Locate and identify every blood parasite.
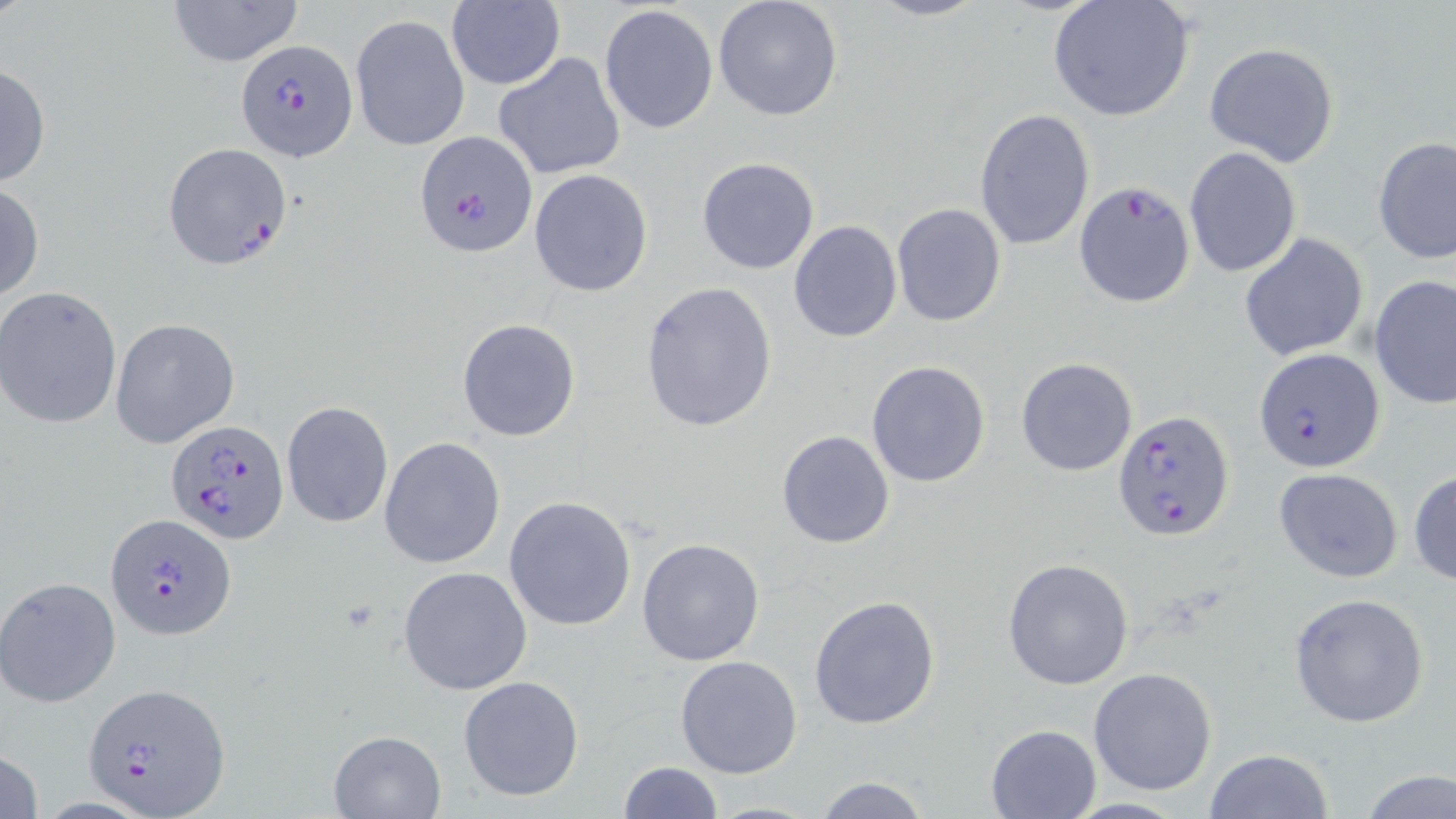
Approximate bounding boxes as named x1/y1/x2/y2 corners in pixels.
Plasmodium falciparum-infected red blood cells: (x1=235, y1=39, x2=357, y2=160), (x1=414, y1=131, x2=539, y2=259), (x1=160, y1=138, x2=292, y2=270), (x1=1074, y1=180, x2=1195, y2=306), (x1=1254, y1=347, x2=1386, y2=473), (x1=1113, y1=409, x2=1234, y2=540), (x1=166, y1=418, x2=290, y2=543), (x1=104, y1=512, x2=234, y2=641), (x1=83, y1=681, x2=230, y2=817).
No Plasmodium ovale, Plasmodium malariae, Plasmodium vivax, Babesia divergens, or Trypanosoma brucei observed.

Summary:
  - Uninfected red blood cell locations: (x1=167, y1=0, x2=305, y2=68), (x1=713, y1=0, x2=843, y2=123), (x1=864, y1=0, x2=987, y2=22), (x1=1047, y1=0, x2=1196, y2=124), (x1=446, y1=1, x2=564, y2=90), (x1=600, y1=4, x2=718, y2=135), (x1=350, y1=13, x2=470, y2=152), (x1=1203, y1=42, x2=1339, y2=168), (x1=493, y1=51, x2=626, y2=180), (x1=0, y1=63, x2=50, y2=188), (x1=974, y1=108, x2=1094, y2=252), (x1=1372, y1=136, x2=1455, y2=264), (x1=1184, y1=147, x2=1302, y2=278), (x1=696, y1=156, x2=821, y2=275), (x1=528, y1=168, x2=654, y2=297), (x1=0, y1=182, x2=45, y2=304), (x1=891, y1=203, x2=1006, y2=325), (x1=788, y1=220, x2=902, y2=341), (x1=1239, y1=232, x2=1369, y2=361), (x1=1369, y1=276, x2=1456, y2=410), (x1=639, y1=281, x2=776, y2=432), (x1=0, y1=285, x2=123, y2=431), (x1=108, y1=318, x2=240, y2=447), (x1=456, y1=318, x2=581, y2=442), (x1=1016, y1=357, x2=1138, y2=477), (x1=866, y1=359, x2=993, y2=488), (x1=281, y1=402, x2=393, y2=526), (x1=775, y1=429, x2=896, y2=549), (x1=380, y1=437, x2=505, y2=570), (x1=1273, y1=467, x2=1403, y2=584), (x1=1409, y1=469, x2=1456, y2=585), (x1=504, y1=495, x2=638, y2=632), (x1=637, y1=537, x2=766, y2=666), (x1=1003, y1=557, x2=1134, y2=689), (x1=398, y1=566, x2=533, y2=696), (x1=0, y1=576, x2=122, y2=707), (x1=1288, y1=592, x2=1431, y2=728), (x1=807, y1=595, x2=940, y2=730), (x1=676, y1=655, x2=803, y2=777), (x1=1088, y1=668, x2=1218, y2=795), (x1=457, y1=675, x2=585, y2=802), (x1=985, y1=723, x2=1100, y2=818), (x1=329, y1=730, x2=444, y2=817), (x1=1, y1=747, x2=43, y2=819), (x1=1204, y1=748, x2=1334, y2=819), (x1=615, y1=760, x2=723, y2=819), (x1=1359, y1=770, x2=1454, y2=819), (x1=812, y1=776, x2=933, y2=819), (x1=702, y1=799, x2=822, y2=817)
  - Slide-level diagnosis: Plasmodium falciparum
  - Magnification: 1000x
  - Field of view: one of a larger specimen
  - Image size: 1456×819 pixels
  - Stain: May-Grünwald-Giemsa
  - Preparation: thin blood smear
  - Modality: light microscopy